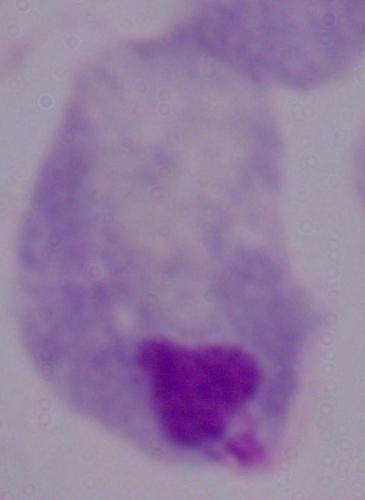
A trichomonad is shown. Captured at 1000x magnification. Photomicrograph.